Give the position of every Plasmodium parasite and every leukocyte.
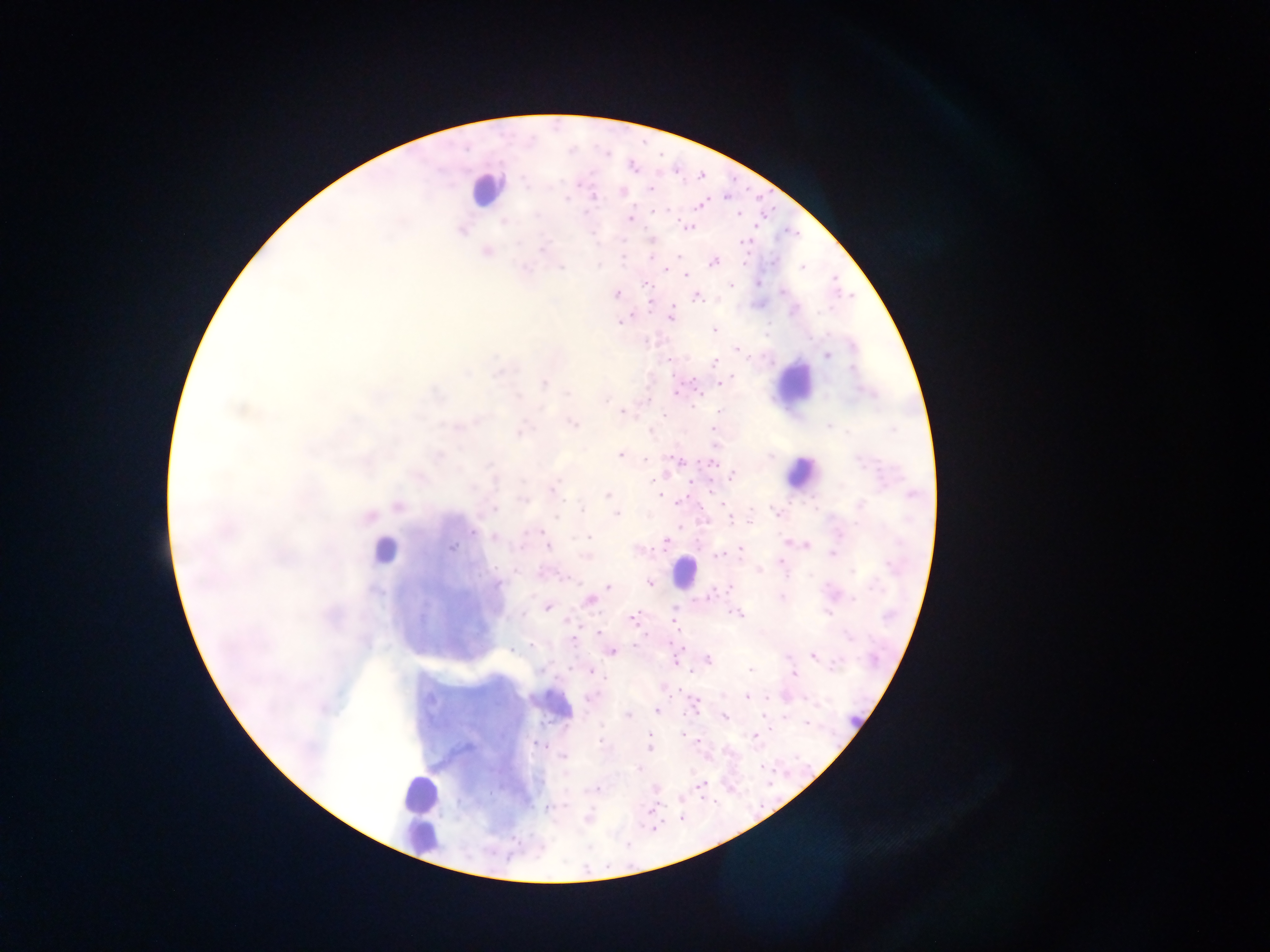
Approximate centers as {x, y} in pixels.
Plasmodium parasites: {645, 143}, {663, 154}, {701, 174}, {526, 182}, {651, 188}, {623, 193}, {567, 200}, {703, 205}, {738, 216}, {631, 219}, {505, 223}, {688, 228}, {463, 231}, {595, 237}, {544, 247}, {486, 250}, {678, 257}, {652, 260}, {713, 262}, {745, 263}, {599, 265}, {561, 266}, {527, 267}, {800, 267}, {683, 273}, {734, 284}, {758, 284}, {646, 285}, {783, 291}, {615, 294}, {696, 297}, {672, 306}, {671, 316}, {621, 323}, {713, 329}, {739, 349}, {827, 356}, {717, 362}, {733, 377}, {544, 383}, {719, 384}, {676, 391}, {567, 394}, {519, 397}, {605, 399}, {622, 410}, {717, 410}, {573, 423}, {828, 425}, {519, 432}, {620, 455}, {769, 457}, {674, 458}, {645, 459}, {687, 462}, {709, 462}, {487, 464}, {859, 465}, {664, 474}, {732, 476}, {495, 484}, {473, 488}, {551, 489}, {607, 495}, {660, 497}, {521, 500}, {681, 502}, {860, 505}, {495, 508}, {583, 510}, {775, 513}, {616, 514}, {556, 518}, {730, 519}, {474, 532}, {589, 535}, {494, 538}, {664, 542}, {786, 543}, {524, 546}, {549, 546}, {808, 547}, {452, 548}, {740, 549}, {831, 552}, {719, 555}, {585, 556}, {783, 563}, {891, 566}, {759, 570}, {851, 573}, {648, 582}, {496, 583}, {607, 586}, {730, 587}, {783, 598}, {852, 599}, {590, 601}, {548, 608}, {739, 614}, {829, 615}, {632, 619}, {674, 624}, {599, 632}, {849, 637}, {573, 641}, {530, 645}, {683, 647}, {515, 649}, {612, 652}, {814, 656}, {705, 662}, {839, 662}, {677, 663}, {592, 671}, {750, 671}, {793, 673}, {592, 697}, {748, 697}, {767, 698}, {433, 703}, {697, 705}, {656, 710}, {627, 716}, {724, 718}, {805, 725}, {683, 736}, {755, 737}, {601, 742}, {538, 743}, {649, 750}, {562, 757}, {763, 767}, {638, 769}, {701, 785}, {770, 785}, {655, 789}, {593, 791}, {682, 800}, {557, 808}, {655, 828}.
Leukocytes: {487, 181}, {790, 384}, {802, 479}, {386, 559}, {681, 575}, {423, 791}, {422, 838}.

Single field of view. Sample from Ghana. Image is 1270×952 pixels. Mobile-phone photograph taken through the microscope. Thick blood smear.